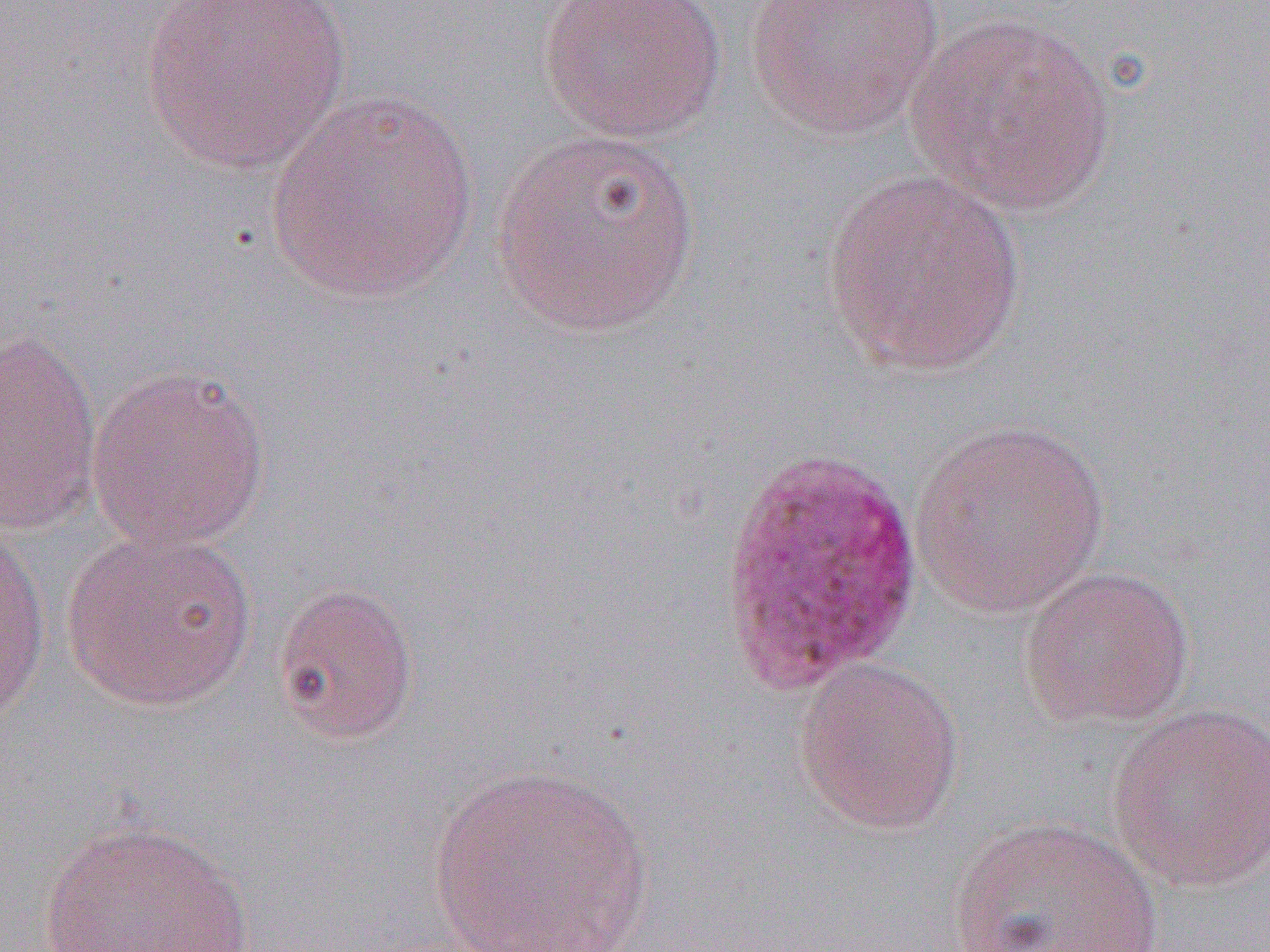
Approximate bounding boxes as named x1/y1/x2/y2 corners in pixels. Plasmodium ovale-infected red blood cell locations: (x1=716, y1=447, x2=924, y2=696). Uninfected red blood cell locations: (x1=536, y1=0, x2=727, y2=143), (x1=746, y1=0, x2=945, y2=139), (x1=139, y1=1, x2=354, y2=176), (x1=902, y1=12, x2=1118, y2=217), (x1=264, y1=89, x2=482, y2=307), (x1=491, y1=127, x2=702, y2=339), (x1=820, y1=168, x2=1031, y2=378), (x1=1, y1=328, x2=103, y2=536), (x1=85, y1=363, x2=272, y2=552), (x1=909, y1=418, x2=1111, y2=618), (x1=0, y1=522, x2=52, y2=725), (x1=61, y1=526, x2=259, y2=712), (x1=1017, y1=563, x2=1195, y2=731), (x1=271, y1=579, x2=420, y2=746), (x1=793, y1=657, x2=965, y2=835), (x1=1105, y1=703, x2=1270, y2=893), (x1=427, y1=761, x2=656, y2=952), (x1=947, y1=815, x2=1163, y2=952), (x1=37, y1=818, x2=257, y2=952). Slide-level diagnosis: Plasmodium ovale. Light microscopy. 1000x magnification. Image is 1270×952 pixels. One field of a larger specimen. Thin blood film.